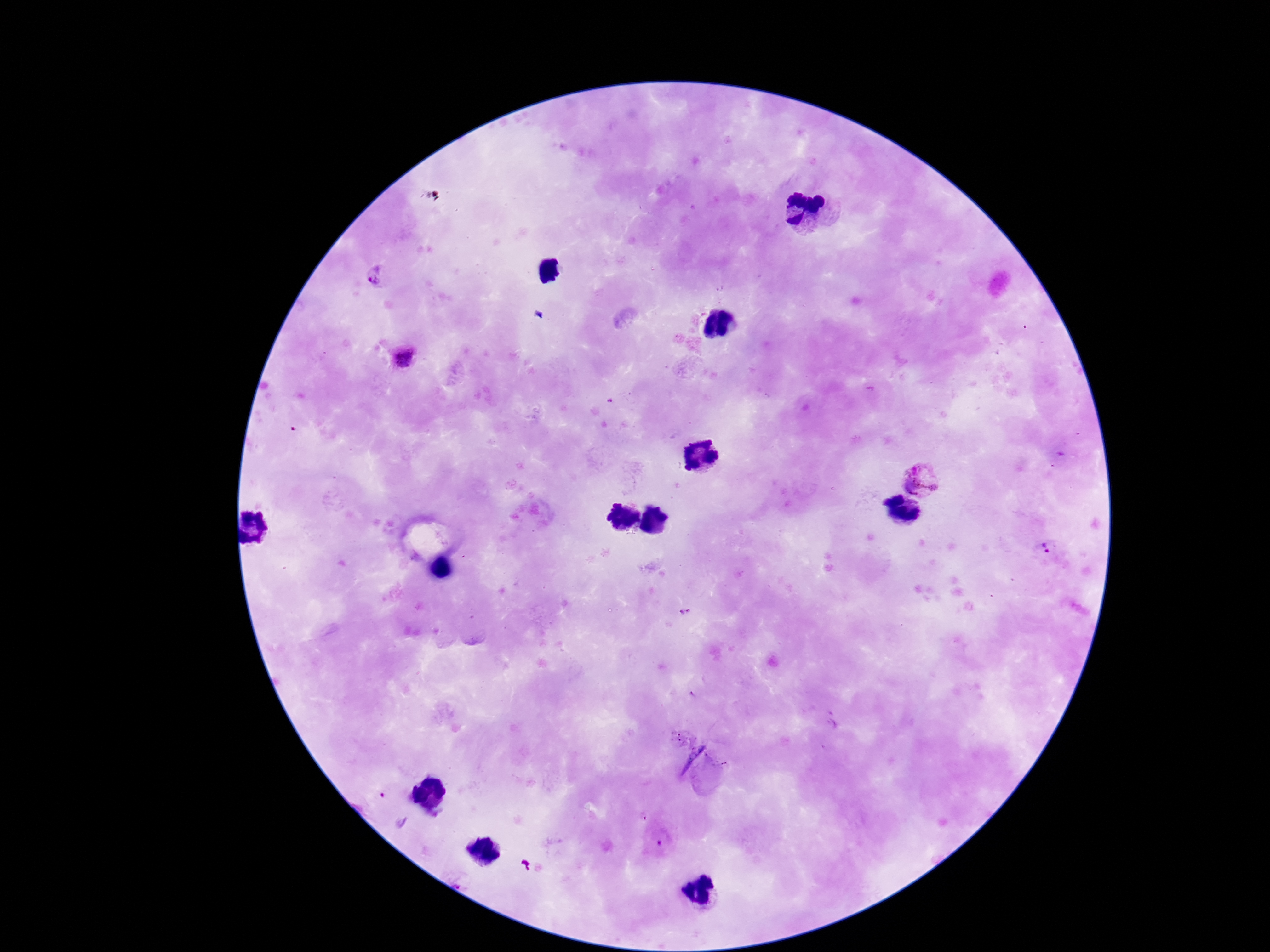

{
  "patient_malaria_status": "infected",
  "stain": "Giemsa",
  "magnification": "100x",
  "capture": "smartphone camera through the microscope eyepiece",
  "plasmodium_parasite_locations": "approximate centers as {x, y} in pixels: {375, 279}, {405, 357}, {921, 478}, {1044, 548}, {686, 611}, {665, 837}",
  "field_of_view": "one from this slide",
  "image_size": "1270×952 pixels",
  "preparation": "thick peripheral-blood smear"
}